Outline each Plasmodium falciparum parasite and classify it by life-cycle stage.
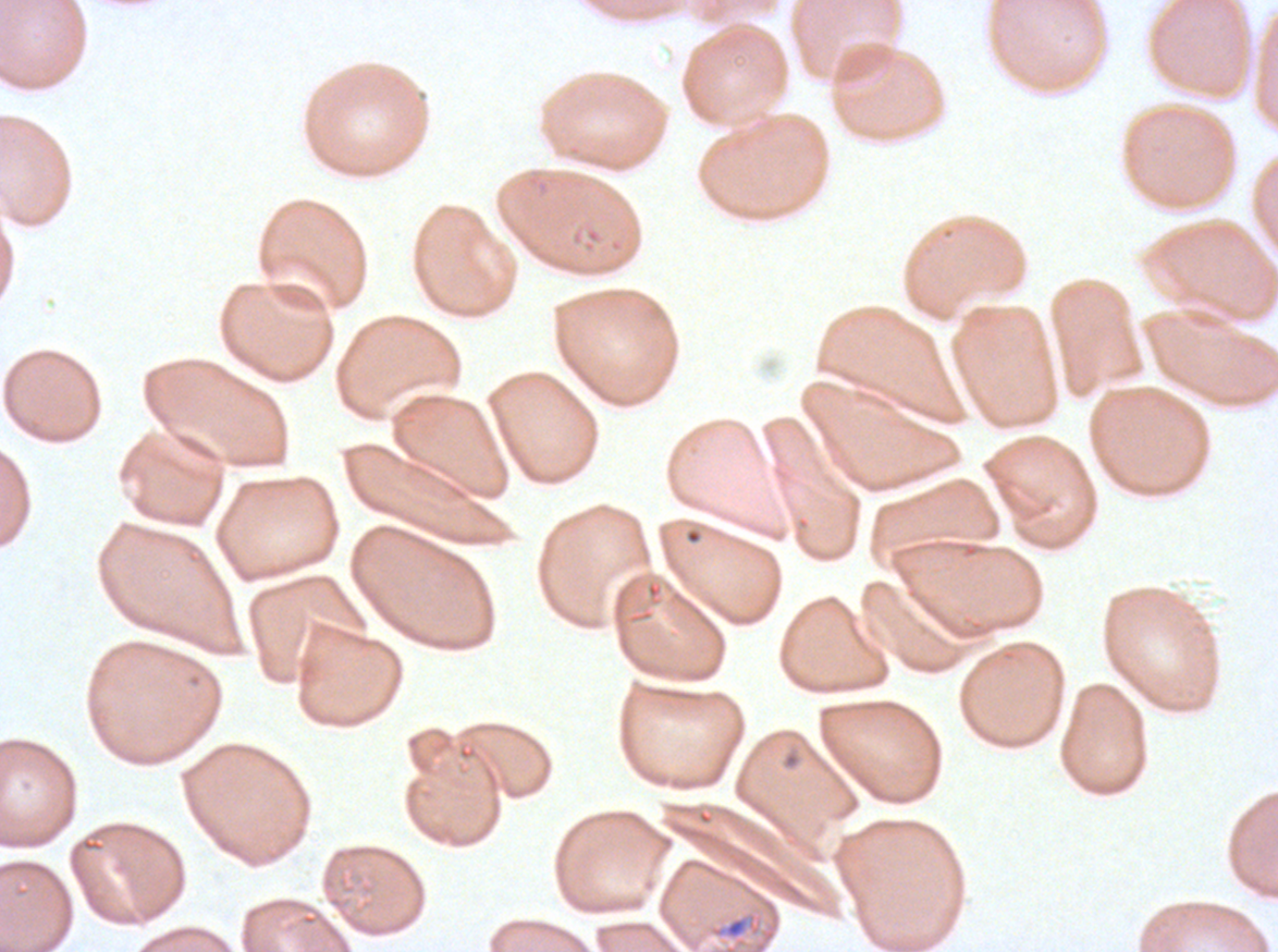
No rings, late-ring/early-trophozoite forms, mid trophozoites, late trophozoites, early schizonts, late schizonts, segmenters, or gametocytes observed.

Approximate bounding boxes as [x1, y1, x2, y2] in pixels. Debris locations: [710, 914, 761, 941]. Image is 1278×952 pixels. Giemsa-stained preparation. Plasmodium falciparum from a patient in The Gambia, cultured ex vivo for 24 to 48 hours. Thin blood film. A sub-image separated from a larger composite.